Report the malaria status of this cell.
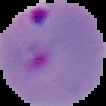

It is parasitized.

image size = 106×106 pixels
preparation = thin blood smear
image type = cell region segmented out of the field of view; surrounding area masked to black